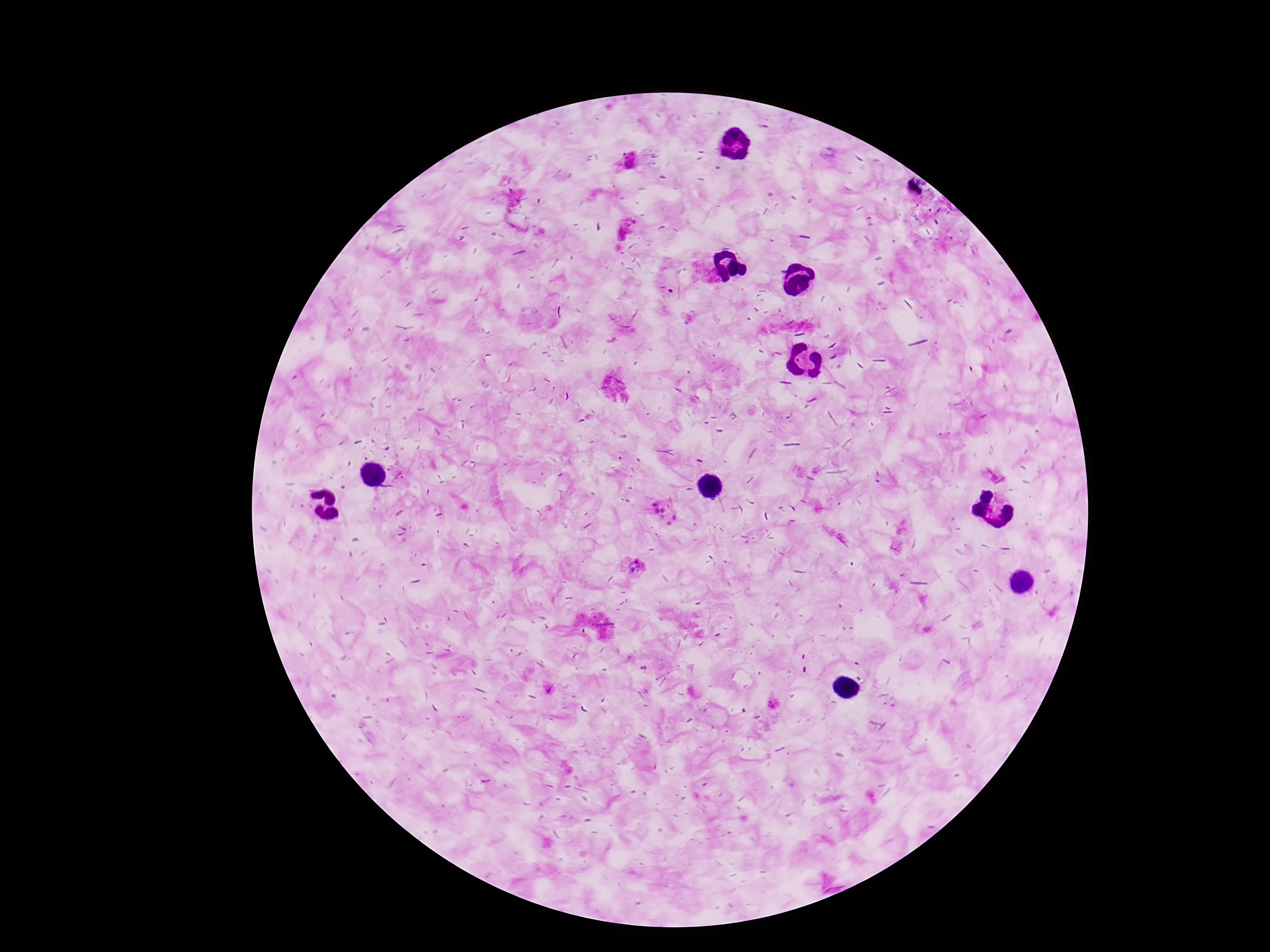
Approximate centers as {x, y} in pixels. Plasmodium parasite locations: {627, 162}, {623, 230}, {665, 514}, {632, 567}. Single field of view. Giemsa-stained preparation. Thick peripheral-blood smear. Patient malaria status: positive. 100x magnification. Smartphone photograph taken through the microscope eyepiece. Image is 1270×952 pixels.